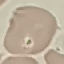

{
  "malaria_status": "uninfected",
  "stain": "Giemsa",
  "capture": "smartphone camera at the microscope eyepiece",
  "preparation": "thin blood film",
  "image_type": "automatically extracted cell patch, resized to 64 × 64 pixels"
}